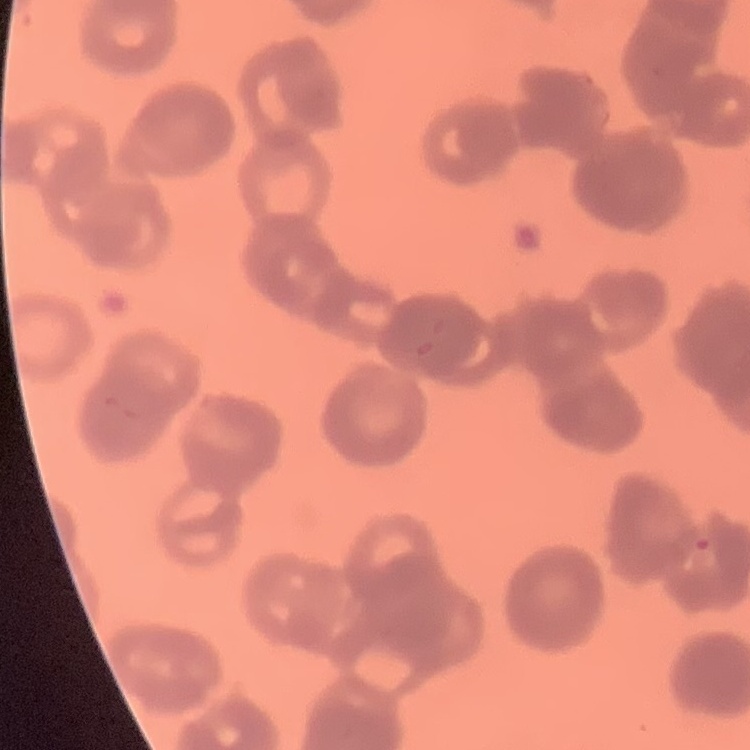
The erythrocytes exhibit rouleaux formation. Thin blood film. Square crop of a larger photomicrograph. Stained with either Field's or Giemsa.